Identify the parasite.
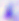
Toxoplasma gondii.

{
  "magnification": "400x",
  "modality": "micrograph"
}